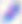 400x magnification. Toxoplasma gondii is shown. Micrograph.